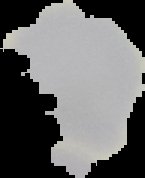

{
  "image_type": "segmented cell region on a black background",
  "malaria_status": "uninfected",
  "image_size": "145×178 pixels",
  "preparation": "thin blood film"
}